Give the extent of the Plasmodium falciparum parasites you find, grouped by life-cycle stage — ring form, trophozoite, schizont, or gametocyte.
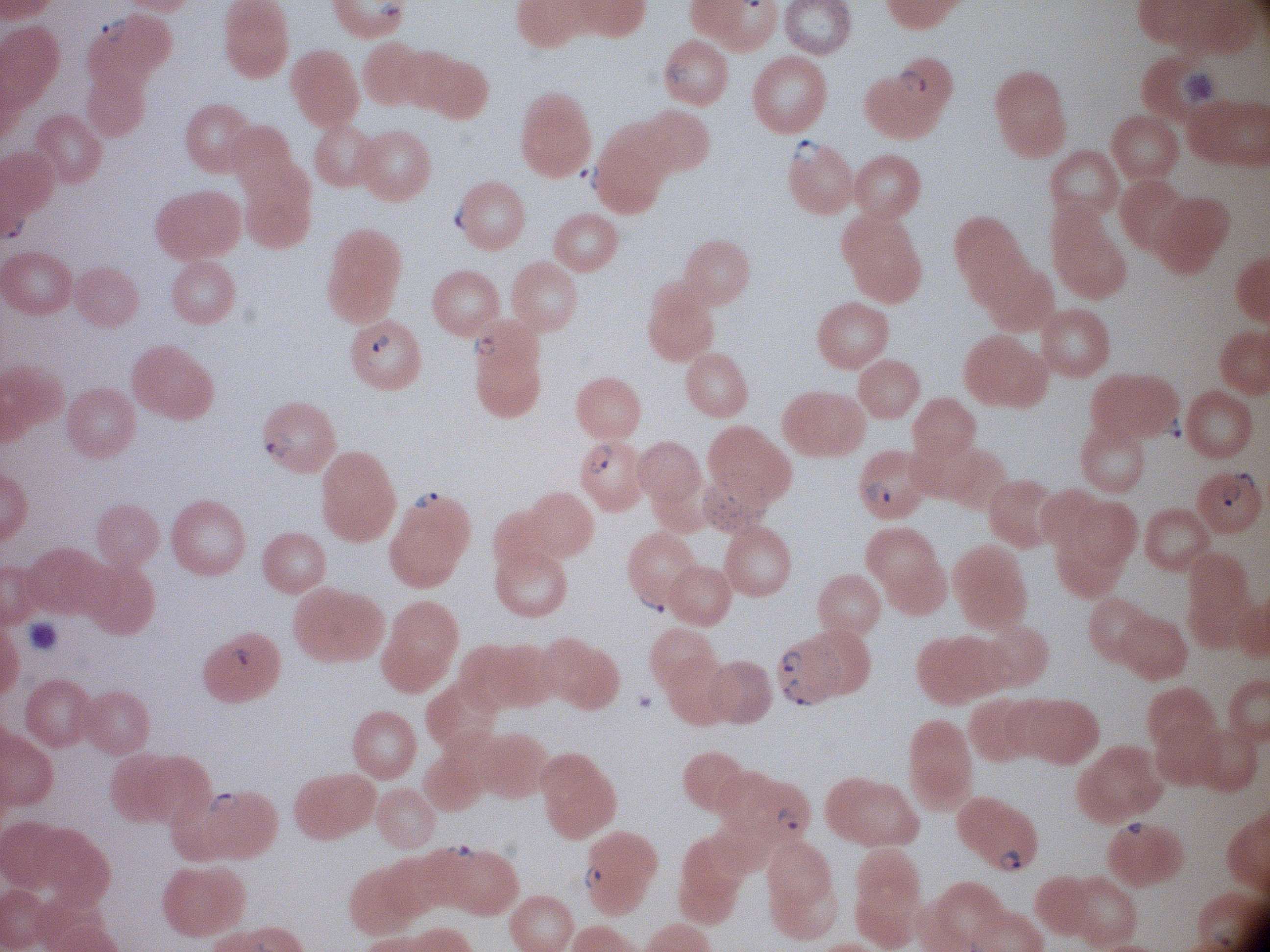
Approximate bounding boxes as (x1, y1, x2, y2) in pixels, from the source annotation, which is not necessarily exhaustive.
Ring forms: (93, 13, 134, 52), (659, 55, 698, 91), (895, 67, 932, 98), (789, 136, 827, 166), (579, 163, 605, 193), (452, 197, 473, 236), (368, 333, 395, 356), (468, 333, 500, 362), (1154, 414, 1188, 442), (259, 430, 296, 464), (586, 441, 617, 478), (1228, 470, 1259, 494), (861, 476, 896, 507), (1215, 484, 1243, 511), (406, 489, 445, 511), (635, 588, 672, 617), (229, 644, 255, 671), (782, 649, 806, 675), (781, 679, 818, 709), (204, 790, 243, 815), (775, 806, 805, 832), (1118, 816, 1150, 841), (445, 841, 481, 861), (995, 844, 1027, 876), (582, 863, 607, 890).

Summary:
  - Microscope: Leica DM2000 with built-in camera
  - Field of view: single
  - Species: Plasmodium falciparum
  - Image size: 1270×952 pixels
  - Preparation: thin blood film
  - Magnification: 100x
  - Stain: Giemsa